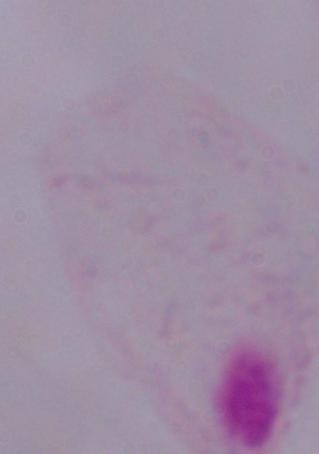

modality = photomicrograph
identification = trichomonad
magnification = 1000x